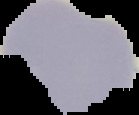

Result: negative for malaria parasites. From a thin blood smear. Segmented cell region on a black background. Image is 139×115 pixels.